Classify this cell by malaria status.
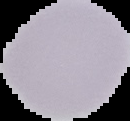

Uninfected.

{
  "preparation": "thin blood film",
  "image_type": "segmented cell region on a black background",
  "image_size": "130×121 pixels"
}